Assess this cell for malaria.
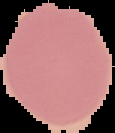

It is uninfected.

From a thin blood smear. Cell region segmented out of the field of view; the surrounding area is masked to black. Image is 115×133 pixels.